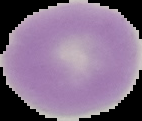

Image is 142×121 pixels. From a thin blood smear. Cell region segmented out of the field of view; the surrounding area is masked to black. Malaria status: uninfected.